Rate the background quality.
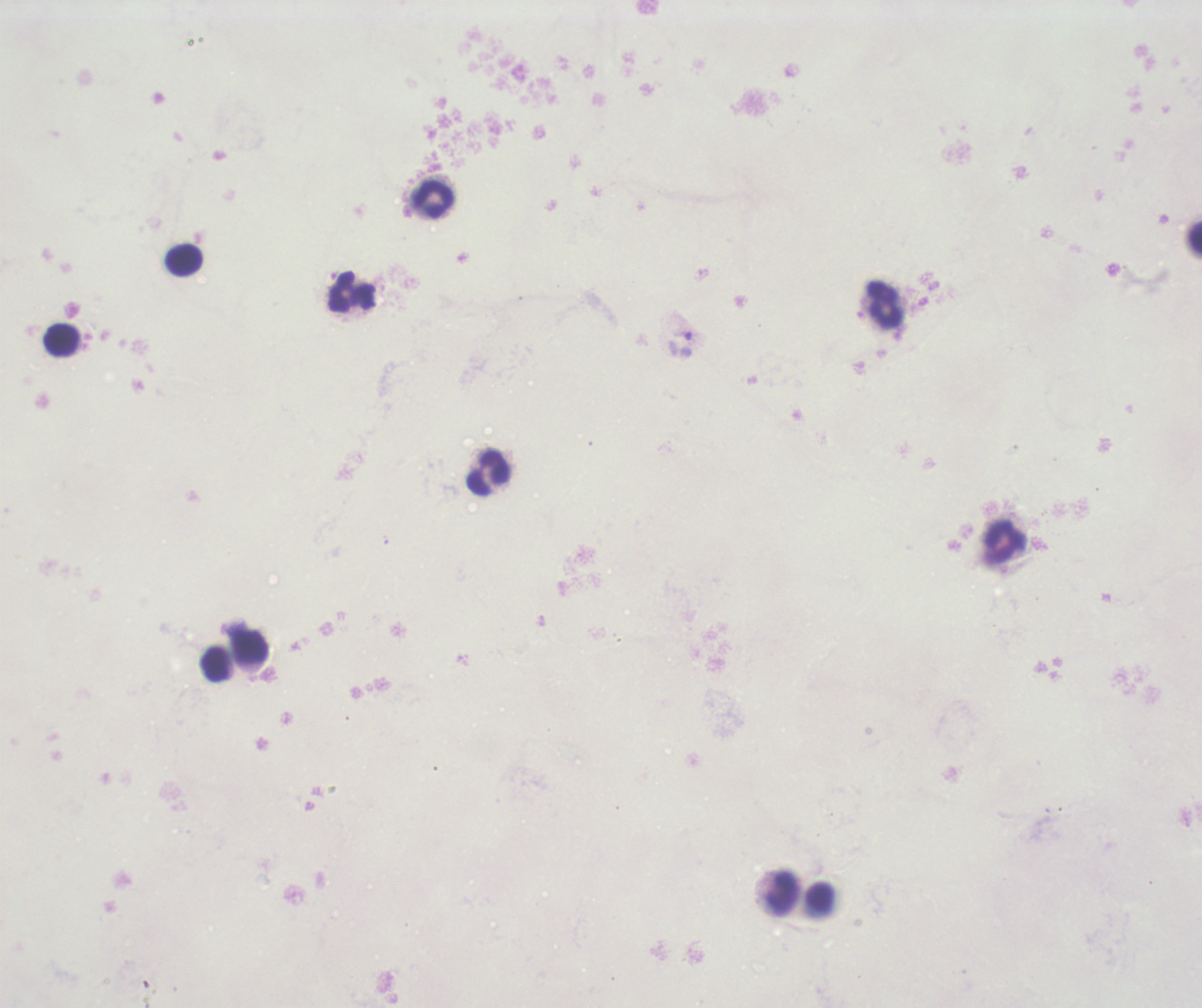
Unsatisfactory.

coordinate format = approximate centers as {x, y} in pixels
trophozoite locations = {682, 335}
leukocyte locations = {433, 200}, {1194, 239}, {183, 260}, {351, 292}, {885, 303}, {61, 341}, {489, 473}, {1004, 543}, {250, 645}, {214, 664}, {781, 893}
context = previously used in a real diagnosis
stain = Romanowsky
preparation = thick smear of blood
result = malaria parasites identified
coloration quality = bad
magnification = 100x
image size = 1202×1008 pixels
field of view = single